Classify this cell by malaria status.
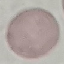
Uninfected.

image type = cell patch, automatically extracted from a larger field of view and resized to 64 × 64 pixels
preparation = thin blood smear
capture = smartphone through the microscope eyepiece
stain = Giemsa